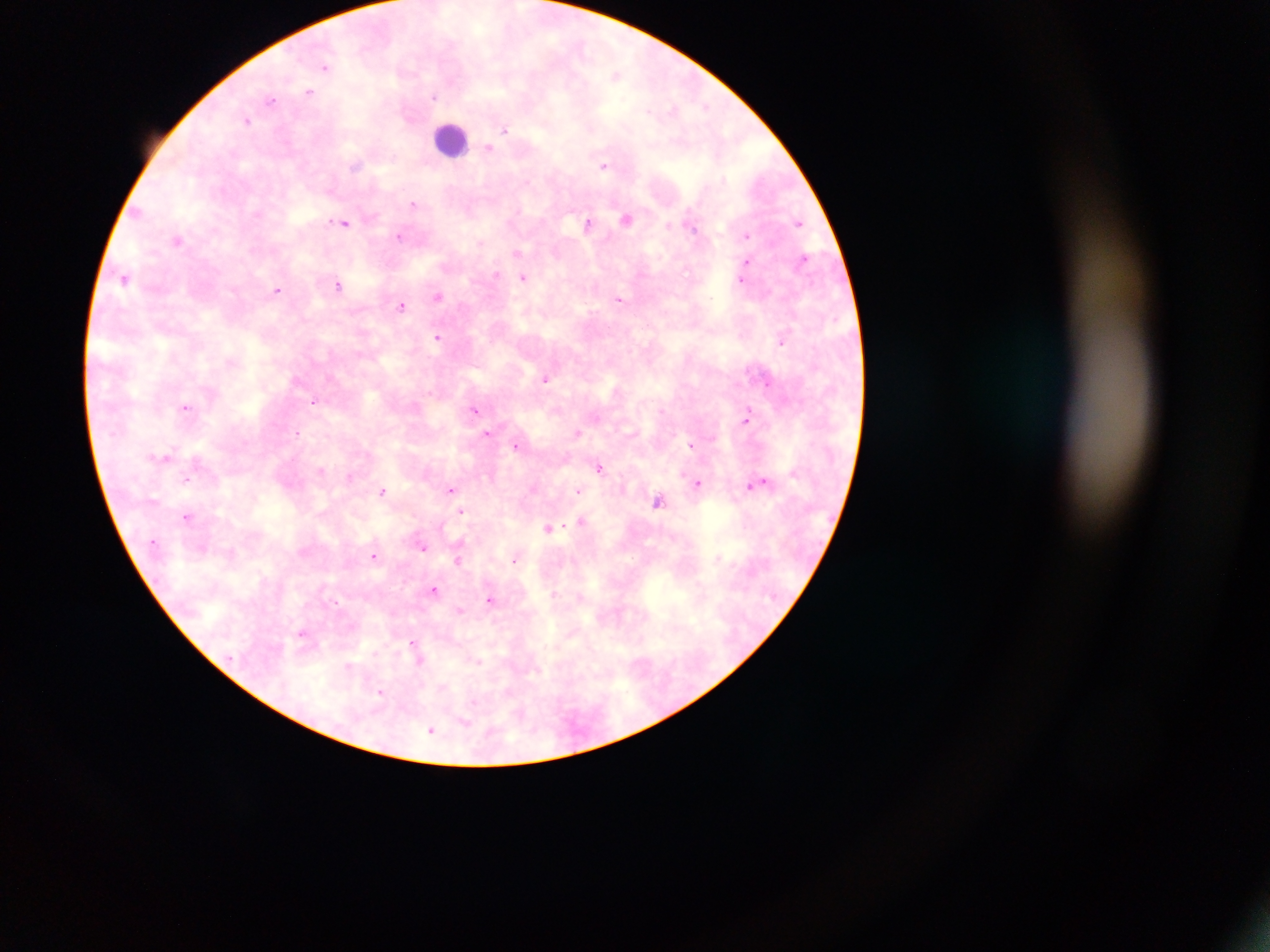

{
  "leukocyte_locations": "approximate centers as [x, y] in pixels: [447, 133]",
  "plasmodium_parasite_locations": "approximate centers as [x, y] in pixels: [326, 67], [309, 91], [434, 94], [271, 99], [249, 121], [505, 129], [490, 147], [603, 165], [414, 203], [344, 223], [798, 223], [589, 224], [748, 235], [400, 237], [517, 254], [748, 262], [123, 278], [524, 278], [741, 281], [339, 286], [277, 290], [439, 295], [620, 298], [402, 306], [438, 338], [782, 342], [546, 379], [766, 383], [315, 401], [186, 407], [475, 409], [747, 420], [297, 432], [490, 432], [577, 434], [517, 447], [692, 448], [600, 468], [187, 478], [763, 480], [698, 482], [746, 482], [451, 488], [384, 489], [579, 490], [659, 502], [462, 511], [185, 517], [581, 521], [549, 528], [423, 549], [376, 557], [458, 559], [514, 560], [434, 589], [556, 594], [489, 599], [459, 609], [301, 631], [412, 641], [380, 692], [433, 730]",
  "image_size": "1270×952 pixels",
  "country": "Ghana",
  "field_of_view": "single",
  "capture": "mobile-phone photograph through a microscope",
  "preparation": "thick blood smear"
}